Report the malaria status of this cell.
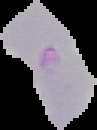
It is uninfected.

Image is 97×130 pixels. The area outside the segmented cell region is set to black. From a thin blood film.